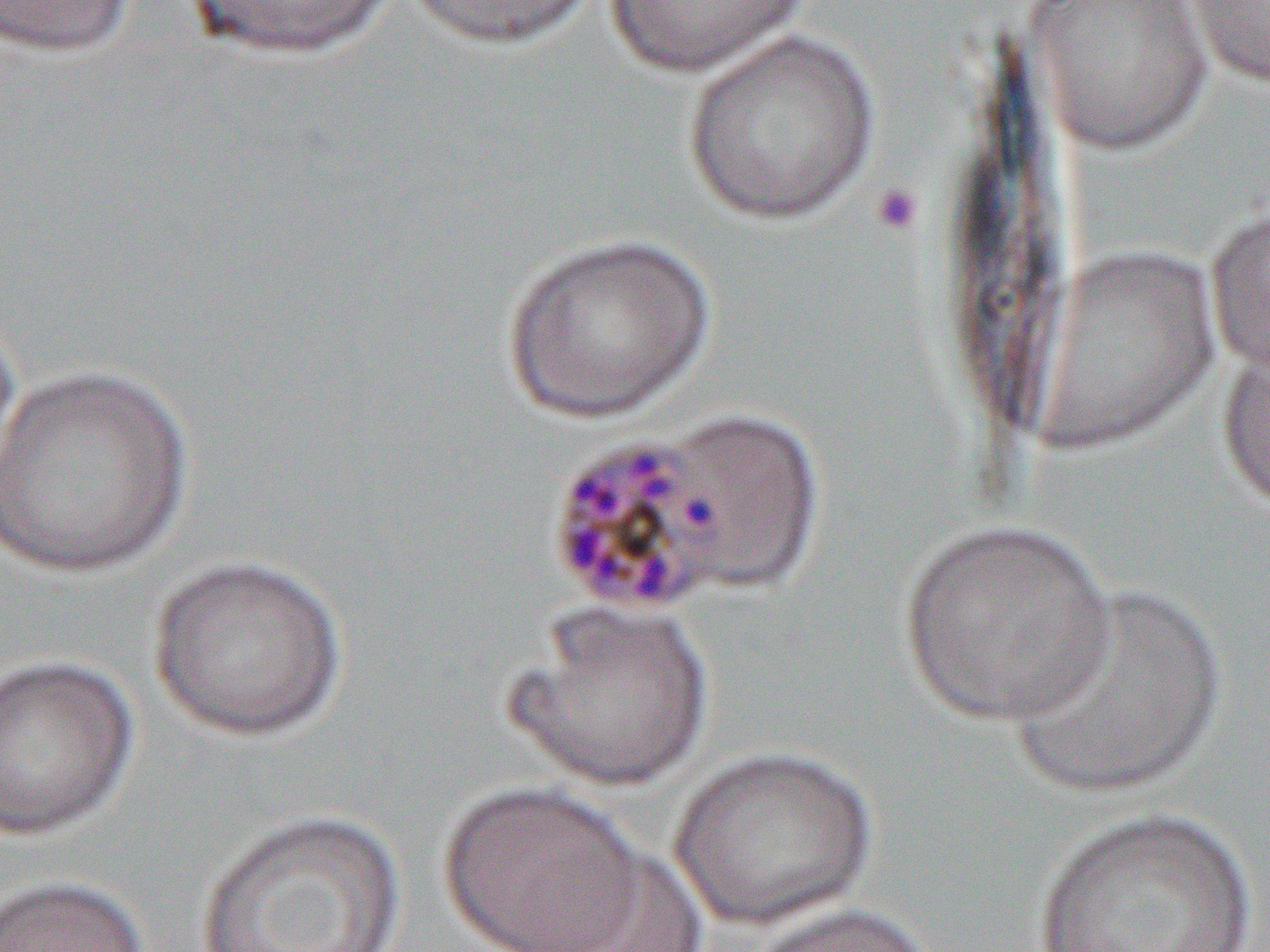

Summary:
  - Coordinate format: approximate bounding boxes as [x1, y1, x2, y2] in pixels
  - Platelet locations: [868, 181, 925, 236]
  - Uninfected red blood cell locations: [0, 0, 138, 58], [402, 0, 598, 51], [597, 0, 818, 76], [1026, 0, 1214, 155], [1180, 0, 1270, 89], [185, 1, 397, 62], [682, 29, 880, 225], [1204, 202, 1270, 379], [502, 230, 716, 423], [0, 294, 25, 496], [1217, 342, 1270, 514], [0, 360, 197, 578], [898, 518, 1114, 726], [147, 554, 348, 741], [1007, 582, 1226, 798], [503, 603, 714, 793], [0, 652, 139, 842], [668, 744, 878, 931], [438, 781, 650, 951], [1033, 806, 1261, 952], [194, 809, 407, 952], [538, 845, 709, 952], [0, 874, 151, 952], [743, 900, 935, 952]
  - Slide-level diagnosis: Plasmodium malariae
  - Preparation: thin blood film
  - Field of view: one of a larger specimen
  - Magnification: 1000x
  - Modality: light microscopy
  - Image size: 1270×952 pixels